Classify this cell by malaria status.
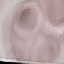

It is uninfected.

preparation = thin smear
image type = cell patch, automatically extracted from a larger field of view and resized to 64 × 64 pixels
capture = smartphone camera at the microscope eyepiece
stain = Giemsa